Identify the parasite.
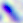

Toxoplasma gondii.

400x magnification. Micrograph.